Describe the morphology of the red blood cells.
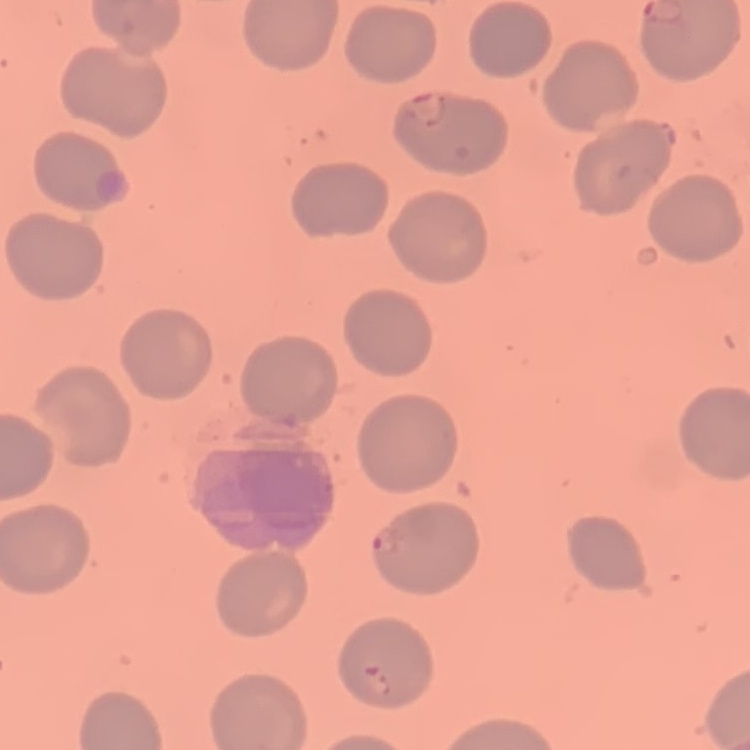
No rouleaux formation.

Summary:
  - Preparation: thin blood smear
  - Image type: one tile cut from a larger photomicrograph
  - Stain: Field's or Giemsa